Classify this cell by malaria status.
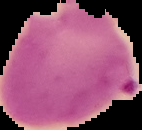

Parasitized.

From a thin blood smear. Segmented cell region on a black background. Image is 142×130 pixels.